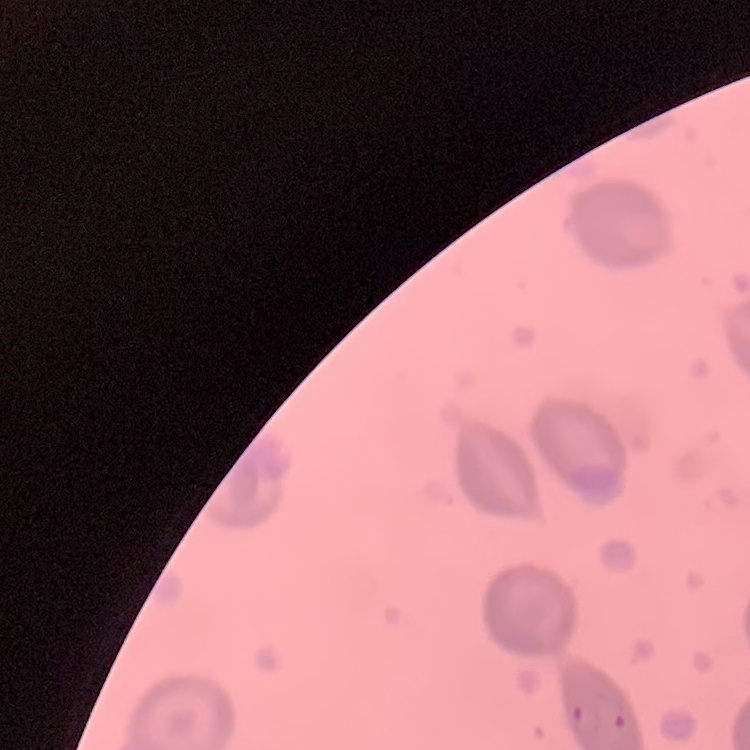
red blood cell morphology = no rouleaux formation
image type = one tile cut from a larger photomicrograph
stain = Field's or Giemsa
preparation = thin blood smear